Describe the morphology of the erythrocytes.
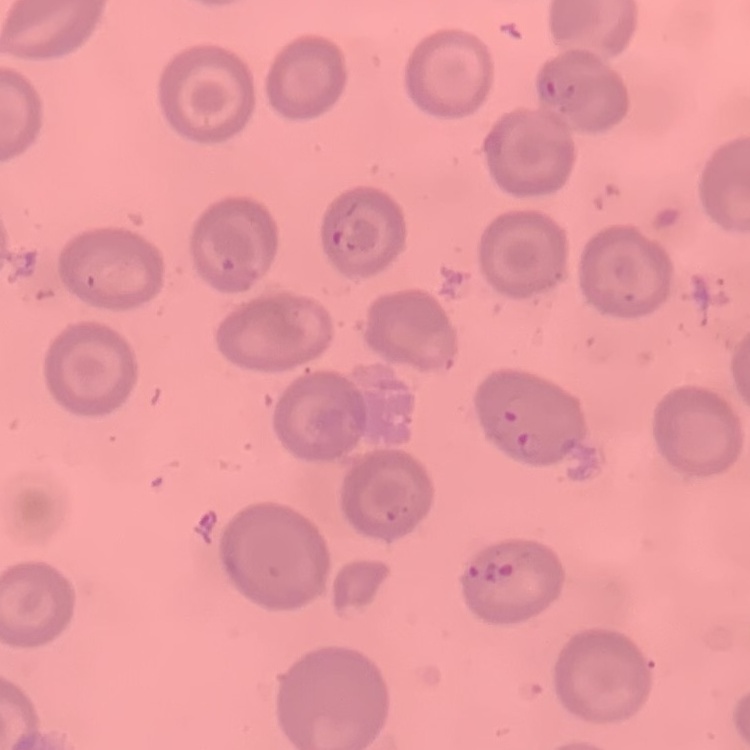

They show no rouleaux formation.

image type = one tile cut from a larger photomicrograph
stain = Field's or Giemsa
preparation = thin blood film